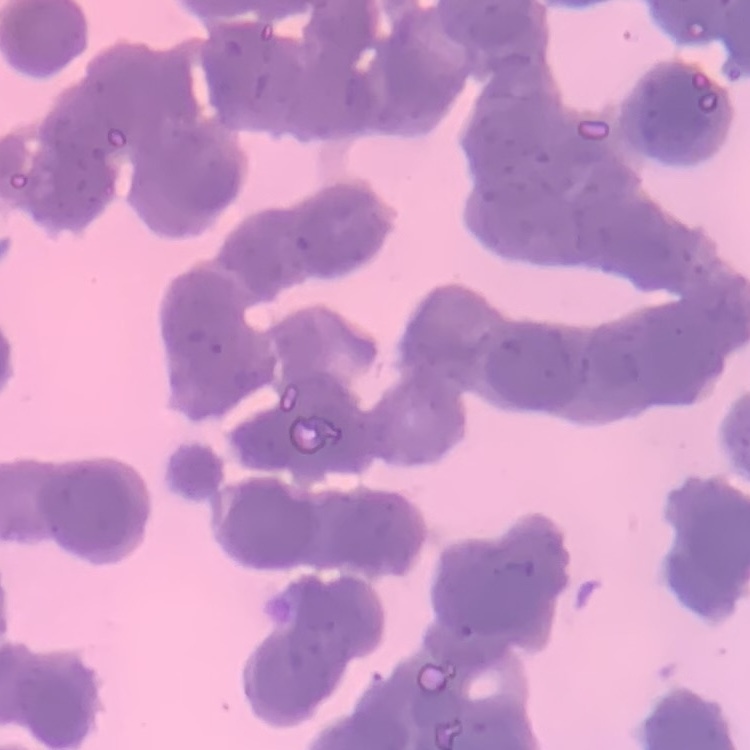

erythrocyte morphology = rouleaux formation
image type = square crop of a larger photomicrograph
stain = Field's or Giemsa
preparation = thin blood smear